Report the malaria status of this cell.
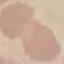
Uninfected.

Acquired by smartphone through the microscope eyepiece. Giemsa stain. Automatically extracted cell patch, resized to 64 × 64 pixels. Thin smear of blood.